Give the preparation type.
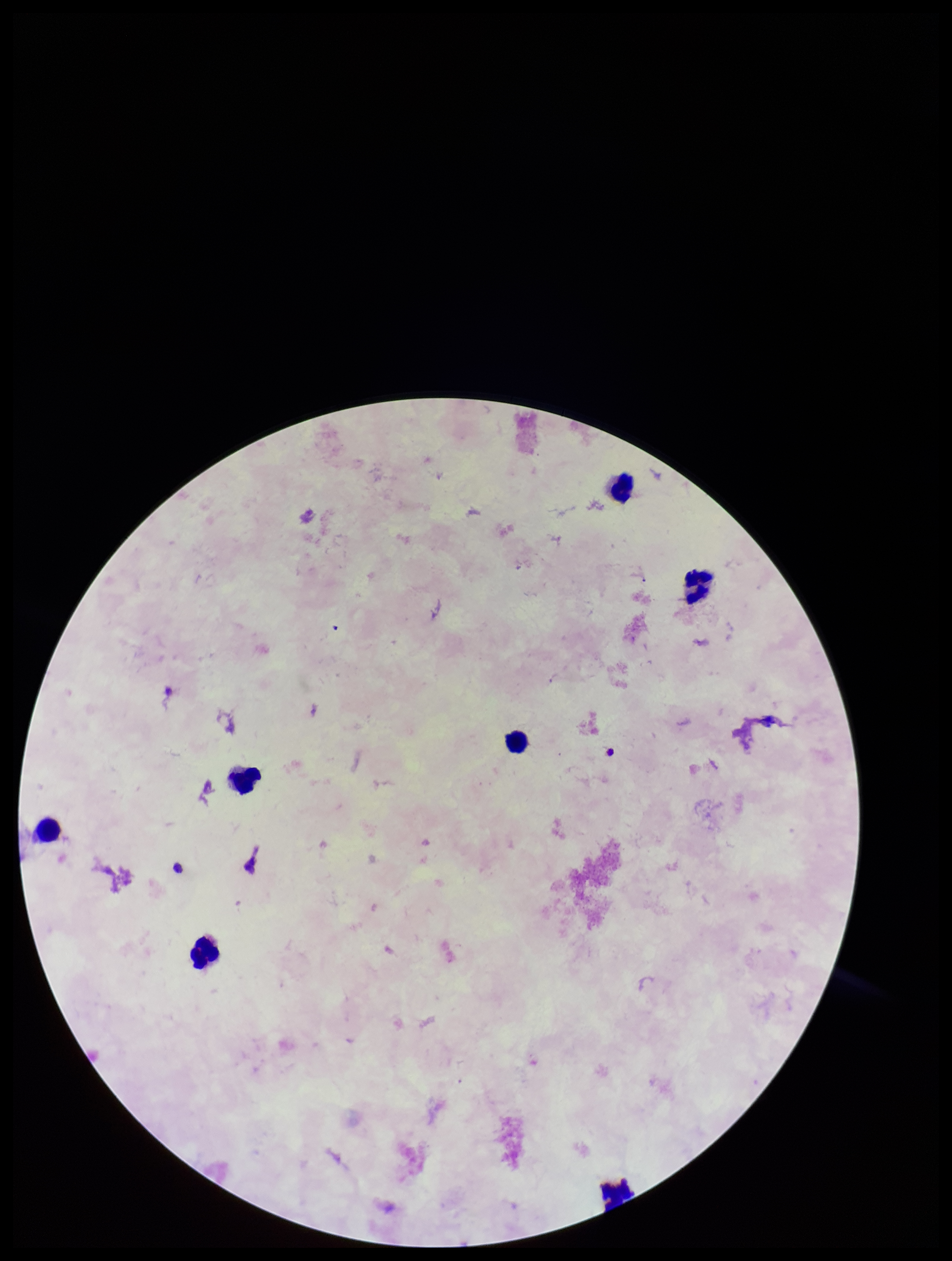

A thick smear.

stain = Giemsa
Plasmodium parasites = none seen
parasite count = 0
patient malaria status = negative
leukocyte count = 7
image size = 952×1261 pixels
field of view = one from this slide
capture = smartphone photograph through the microscope eyepiece